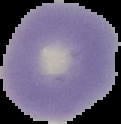

From a thin blood smear. Malaria status: uninfected. The area outside the segmented cell region is set to black. Image is 121×124 pixels.